State which parasite is depicted.
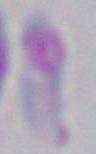
Toxoplasma gondii.

Summary:
  - Modality: photomicrograph
  - Magnification: 1000x